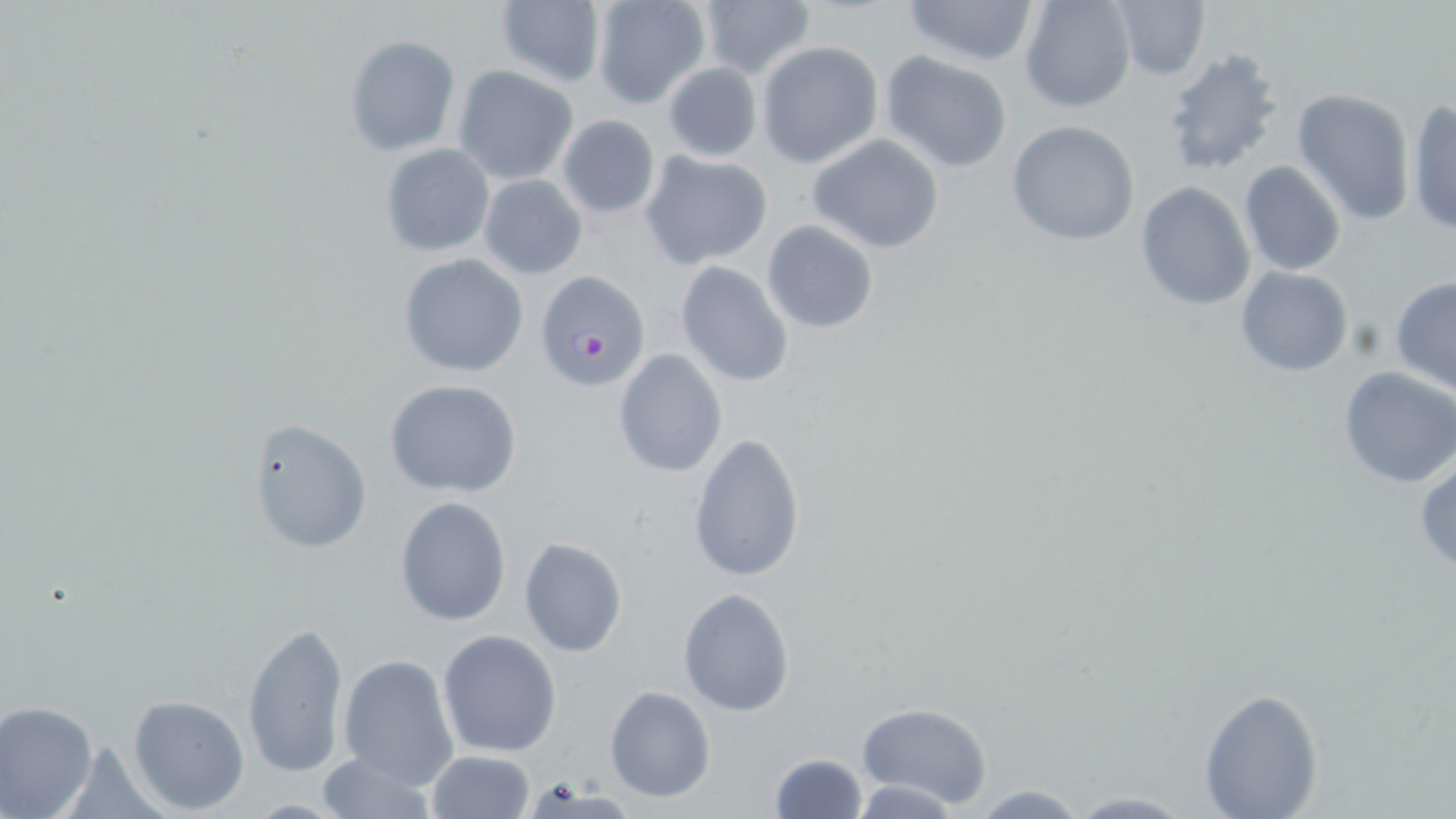
slide-level diagnosis = Plasmodium falciparum
magnification = 1000x
stain = May-Grünwald-Giemsa
modality = optical microscopy
image size = 1456×819 pixels
preparation = thin blood film
Plasmodium falciparum-infected red blood cell locations = approximate bounding boxes as (x1, y1, x2, y2) in pixels: (533, 271, 652, 393)
uninfected red blood cell locations = approximate bounding boxes as (x1, y1, x2, y2) in pixels: (492, 0, 606, 90), (589, 0, 712, 110), (903, 0, 1039, 70), (1018, 0, 1137, 113), (1106, 0, 1212, 82), (693, 2, 815, 78), (342, 33, 462, 158), (757, 41, 882, 168), (1162, 47, 1287, 174), (881, 50, 1015, 173), (661, 61, 762, 162), (452, 65, 578, 185), (1290, 87, 1418, 226), (1406, 98, 1455, 235), (555, 114, 661, 219), (1006, 119, 1142, 247), (807, 133, 945, 255), (379, 143, 496, 258), (643, 151, 774, 268), (1237, 161, 1347, 277), (478, 175, 587, 279), (1135, 182, 1256, 313), (761, 219, 879, 334), (398, 254, 529, 376), (675, 261, 795, 388), (1235, 267, 1355, 378), (1389, 275, 1456, 395), (614, 349, 728, 478), (1337, 366, 1456, 487), (385, 380, 523, 499), (247, 417, 373, 556), (687, 431, 807, 586), (1415, 459, 1456, 572), (394, 495, 512, 627), (518, 537, 628, 658), (678, 587, 795, 716), (240, 620, 349, 779), (438, 629, 562, 757), (337, 653, 460, 790), (604, 685, 716, 803), (1197, 686, 1325, 818), (126, 693, 251, 815), (0, 700, 100, 818), (854, 702, 993, 810), (427, 750, 536, 818), (315, 751, 439, 819), (767, 751, 868, 819), (965, 784, 1093, 817), (1060, 792, 1199, 818)
field of view = single